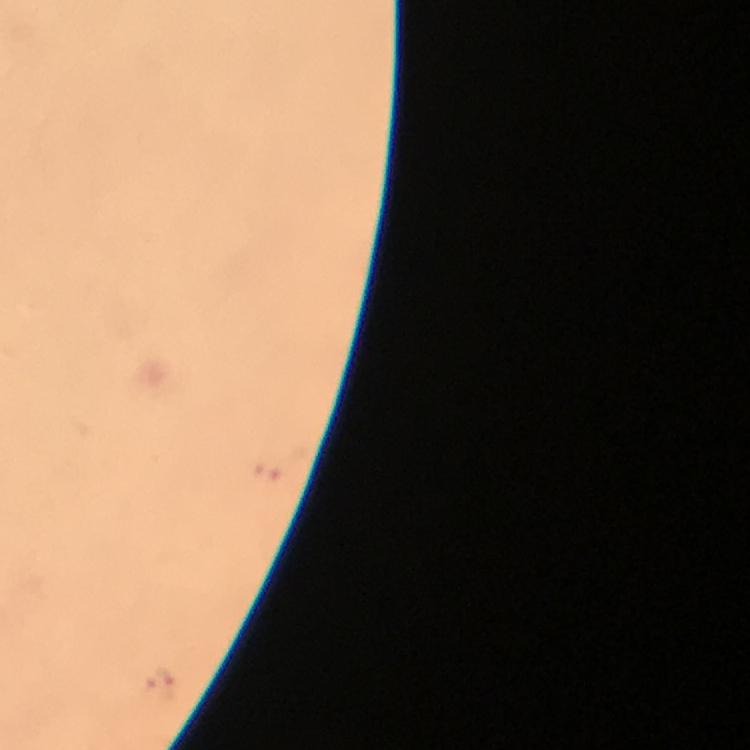 Approximate centers as {x, y} in pixels. Malaria parasite locations: {160, 686}. From a diagnostic examination for malaria. A crop from one field of view. Photographed through the microscope with a smartphone camera. Image is 750×750 pixels. Giemsa-stained preparation. Immersion oil applied. 100x magnification. Thick blood film.